Name the parasite shown.
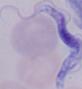

This is a trypanosome.

magnification: 1000x
modality: photomicrograph